Locate every blood parasite and identify its species.
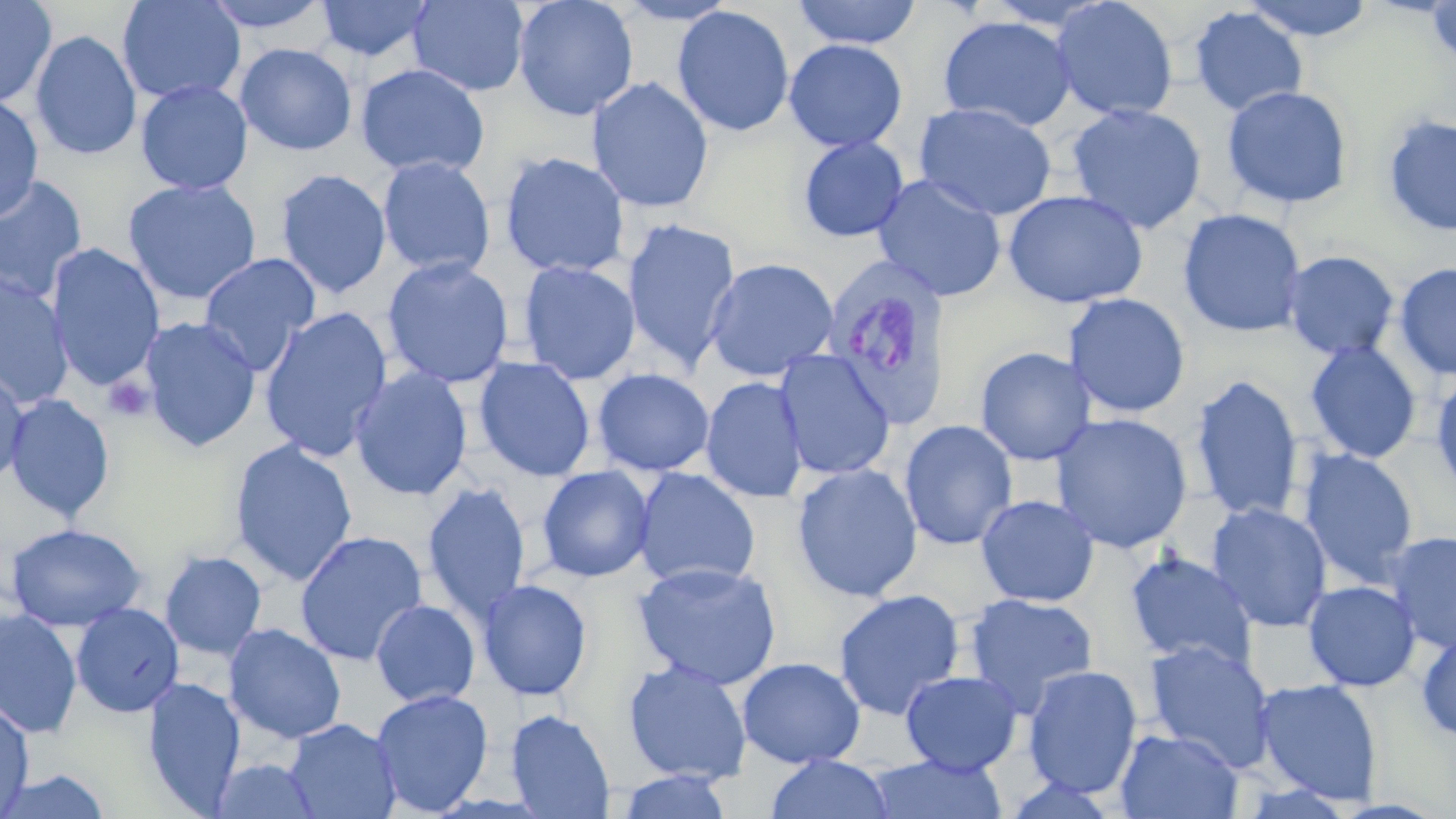
Approximate bounding boxes as named x1/y1/x2/y2 corners in pixels.
Plasmodium vivax-infected red blood cells: (x1=821, y1=258, x2=954, y2=429).
No Plasmodium falciparum, Plasmodium ovale, Plasmodium malariae, Babesia divergens, or Trypanosoma brucei observed.

Summary:
  - Platelet locations: (x1=102, y1=375, x2=153, y2=422)
  - Uninfected red blood cell locations: (x1=0, y1=0, x2=57, y2=108), (x1=117, y1=0, x2=246, y2=105), (x1=200, y1=0, x2=333, y2=33), (x1=315, y1=0, x2=436, y2=62), (x1=408, y1=0, x2=530, y2=96), (x1=512, y1=0, x2=639, y2=121), (x1=613, y1=0, x2=740, y2=25), (x1=792, y1=0, x2=922, y2=49), (x1=1051, y1=0, x2=1178, y2=122), (x1=1239, y1=0, x2=1378, y2=42), (x1=1425, y1=1, x2=1456, y2=72), (x1=672, y1=6, x2=796, y2=138), (x1=1188, y1=6, x2=1308, y2=117), (x1=938, y1=15, x2=1076, y2=132), (x1=30, y1=29, x2=142, y2=161), (x1=783, y1=39, x2=907, y2=153), (x1=234, y1=43, x2=357, y2=156), (x1=355, y1=64, x2=490, y2=179), (x1=587, y1=77, x2=714, y2=213), (x1=135, y1=79, x2=254, y2=195), (x1=1222, y1=85, x2=1353, y2=209), (x1=0, y1=94, x2=44, y2=222), (x1=914, y1=101, x2=1057, y2=221), (x1=1065, y1=103, x2=1207, y2=234), (x1=1382, y1=113, x2=1456, y2=238), (x1=797, y1=136, x2=909, y2=242), (x1=499, y1=151, x2=630, y2=278), (x1=376, y1=156, x2=496, y2=278), (x1=274, y1=168, x2=392, y2=299), (x1=872, y1=174, x2=1007, y2=302), (x1=0, y1=175, x2=89, y2=304), (x1=123, y1=177, x2=262, y2=305), (x1=1002, y1=189, x2=1149, y2=310), (x1=1177, y1=208, x2=1307, y2=338), (x1=622, y1=218, x2=741, y2=371), (x1=45, y1=243, x2=165, y2=392), (x1=1281, y1=250, x2=1400, y2=361), (x1=198, y1=252, x2=322, y2=375), (x1=381, y1=256, x2=515, y2=389), (x1=704, y1=257, x2=839, y2=381), (x1=517, y1=260, x2=640, y2=385), (x1=1393, y1=262, x2=1456, y2=379), (x1=0, y1=274, x2=74, y2=407), (x1=1063, y1=293, x2=1191, y2=419), (x1=259, y1=306, x2=394, y2=461), (x1=138, y1=316, x2=262, y2=452), (x1=1304, y1=341, x2=1422, y2=464), (x1=974, y1=346, x2=1096, y2=466), (x1=774, y1=350, x2=895, y2=480), (x1=473, y1=357, x2=596, y2=482), (x1=349, y1=367, x2=473, y2=501), (x1=0, y1=368, x2=30, y2=488), (x1=592, y1=368, x2=715, y2=476), (x1=1430, y1=368, x2=1456, y2=500), (x1=1190, y1=374, x2=1304, y2=523), (x1=701, y1=376, x2=808, y2=503), (x1=3, y1=393, x2=115, y2=521), (x1=1050, y1=412, x2=1193, y2=553), (x1=899, y1=420, x2=1018, y2=550), (x1=229, y1=439, x2=358, y2=586), (x1=1297, y1=449, x2=1419, y2=588), (x1=791, y1=463, x2=923, y2=602), (x1=536, y1=465, x2=655, y2=582), (x1=632, y1=468, x2=761, y2=590), (x1=422, y1=482, x2=531, y2=624), (x1=976, y1=494, x2=1099, y2=608), (x1=1207, y1=502, x2=1332, y2=633), (x1=4, y1=522, x2=147, y2=632), (x1=294, y1=530, x2=428, y2=666), (x1=1384, y1=531, x2=1456, y2=652), (x1=160, y1=550, x2=267, y2=660), (x1=1124, y1=551, x2=1258, y2=670), (x1=633, y1=561, x2=781, y2=690), (x1=478, y1=579, x2=593, y2=701), (x1=1303, y1=580, x2=1420, y2=691), (x1=833, y1=588, x2=966, y2=721), (x1=964, y1=593, x2=1099, y2=714), (x1=371, y1=600, x2=480, y2=707), (x1=71, y1=602, x2=184, y2=717), (x1=0, y1=608, x2=82, y2=739), (x1=223, y1=623, x2=346, y2=743), (x1=1416, y1=625, x2=1456, y2=742), (x1=1144, y1=639, x2=1277, y2=771), (x1=737, y1=657, x2=865, y2=769), (x1=622, y1=659, x2=752, y2=785), (x1=1022, y1=665, x2=1143, y2=798), (x1=900, y1=671, x2=1023, y2=775), (x1=143, y1=676, x2=245, y2=814), (x1=1254, y1=678, x2=1384, y2=804), (x1=371, y1=688, x2=493, y2=816), (x1=1, y1=698, x2=34, y2=816), (x1=506, y1=709, x2=615, y2=819), (x1=283, y1=717, x2=401, y2=819), (x1=1115, y1=727, x2=1242, y2=818), (x1=764, y1=754, x2=895, y2=818), (x1=864, y1=754, x2=1008, y2=818), (x1=210, y1=758, x2=320, y2=818), (x1=0, y1=768, x2=112, y2=818), (x1=618, y1=770, x2=732, y2=818)
  - Slide-level diagnosis: Plasmodium vivax
  - Field of view: single
  - Modality: light microscopy
  - Stain: May-Grünwald-Giemsa
  - Image size: 1456×819 pixels
  - Preparation: thin blood smear
  - Magnification: 1000x